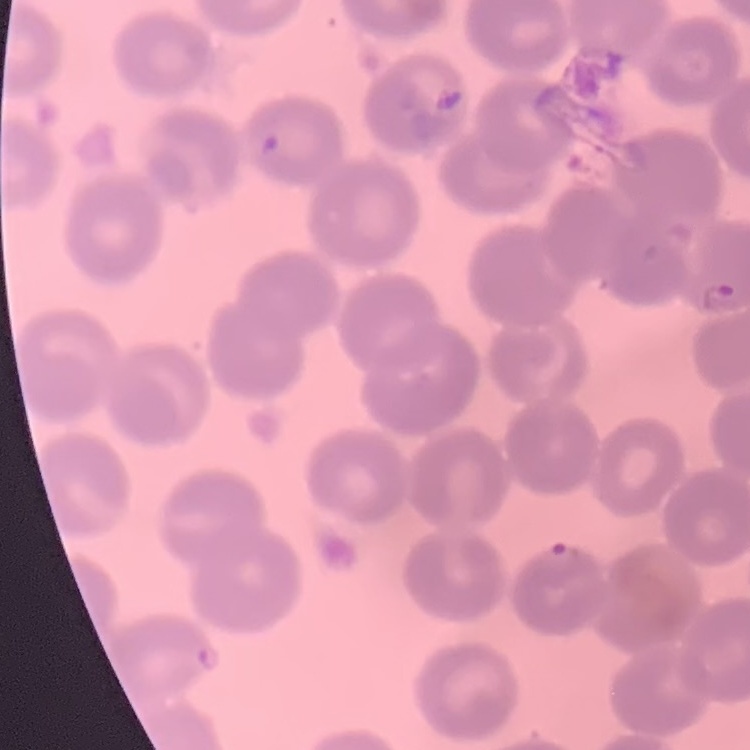

red_blood_cell_morphology: no rouleaux formation
preparation: thin blood smear
image_type: one tile cut from a larger photomicrograph
stain: Field's or Giemsa